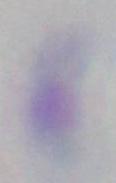 Photomicrograph. Toxoplasma gondii is shown. Captured at 1000x magnification.